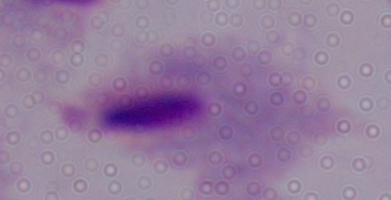
identification = trichomonad
modality = photomicrograph
magnification = 1000x